Locate every malaria parasite and identify its life-cycle stage.
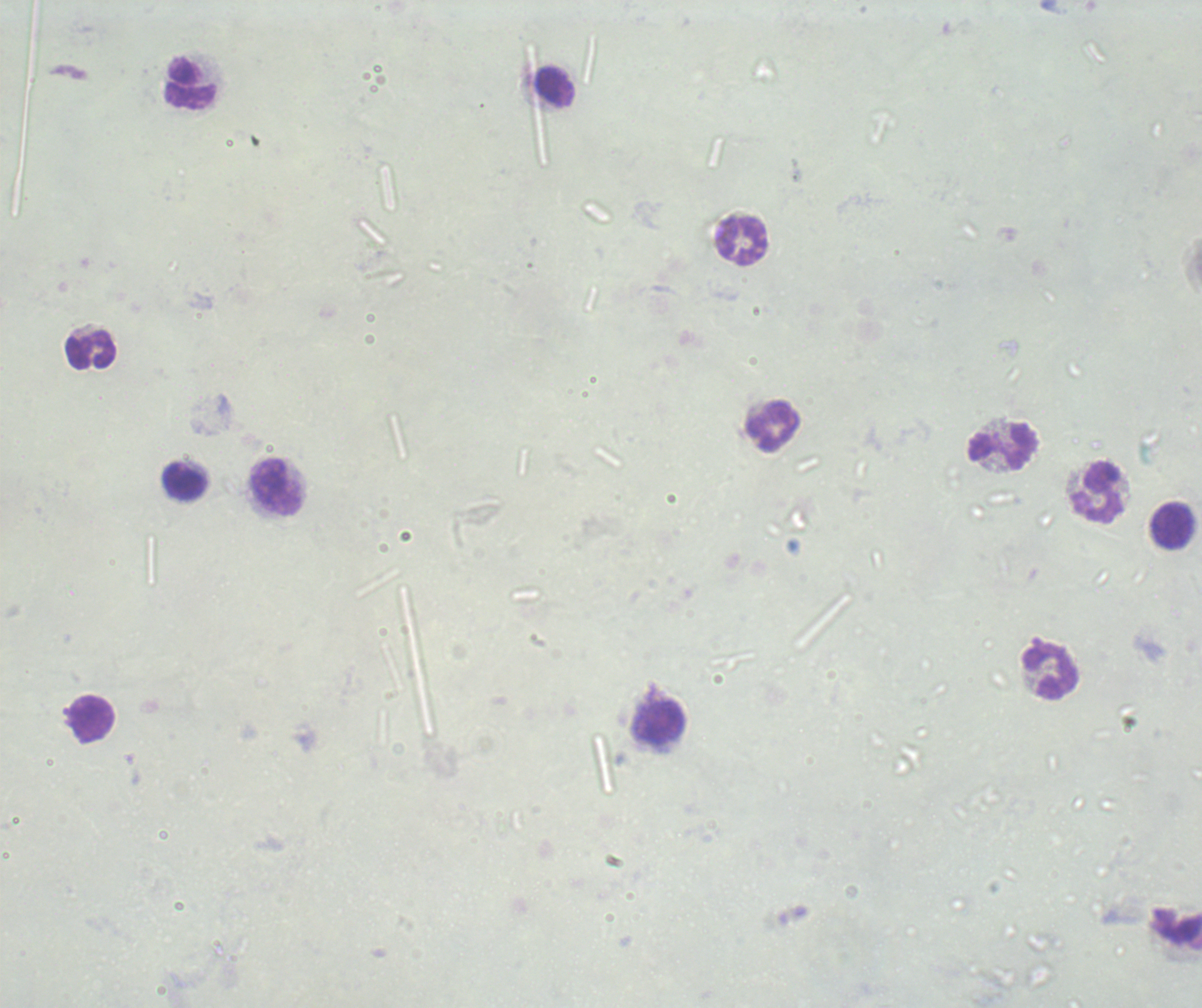
No malaria parasites seen.

Approximate centers as (x, y) in pixels. Leukocyte locations: (191, 84), (553, 87), (743, 242), (91, 351), (773, 427), (1002, 448), (185, 483), (277, 488), (1099, 493), (1172, 526), (1051, 671), (93, 719), (659, 723). Previously used in an actual diagnosis. Thick smear of blood. Captured at 100x magnification. Background quality: poor. Romanowsky stain. One field from this slide. Image is 1202×1008 pixels.